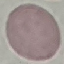

Summary:
  - Result: no malaria parasites seen
  - Capture: smartphone through the microscope eyepiece
  - Stain: Giemsa
  - Image type: cell patch, automatically extracted from a larger field of view and resized to 64 × 64 pixels
  - Preparation: thin blood smear